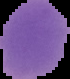
Image is 70×79 pixels. Malaria status: uninfected. From a thin blood smear. The area outside the segmented cell region is set to black.